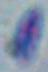
magnification = 1000x
modality = micrograph
identification = Toxoplasma gondii